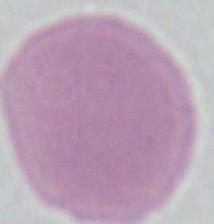

Summary:
  - Identification: erythrocyte
  - Modality: micrograph
  - Magnification: 1000x